State which parasite is depicted.
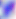

This is Toxoplasma gondii.

magnification = 400x
modality = photomicrograph